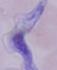
1000x magnification. Micrograph. A trypanosome is seen.